Identify the blood parasite species.
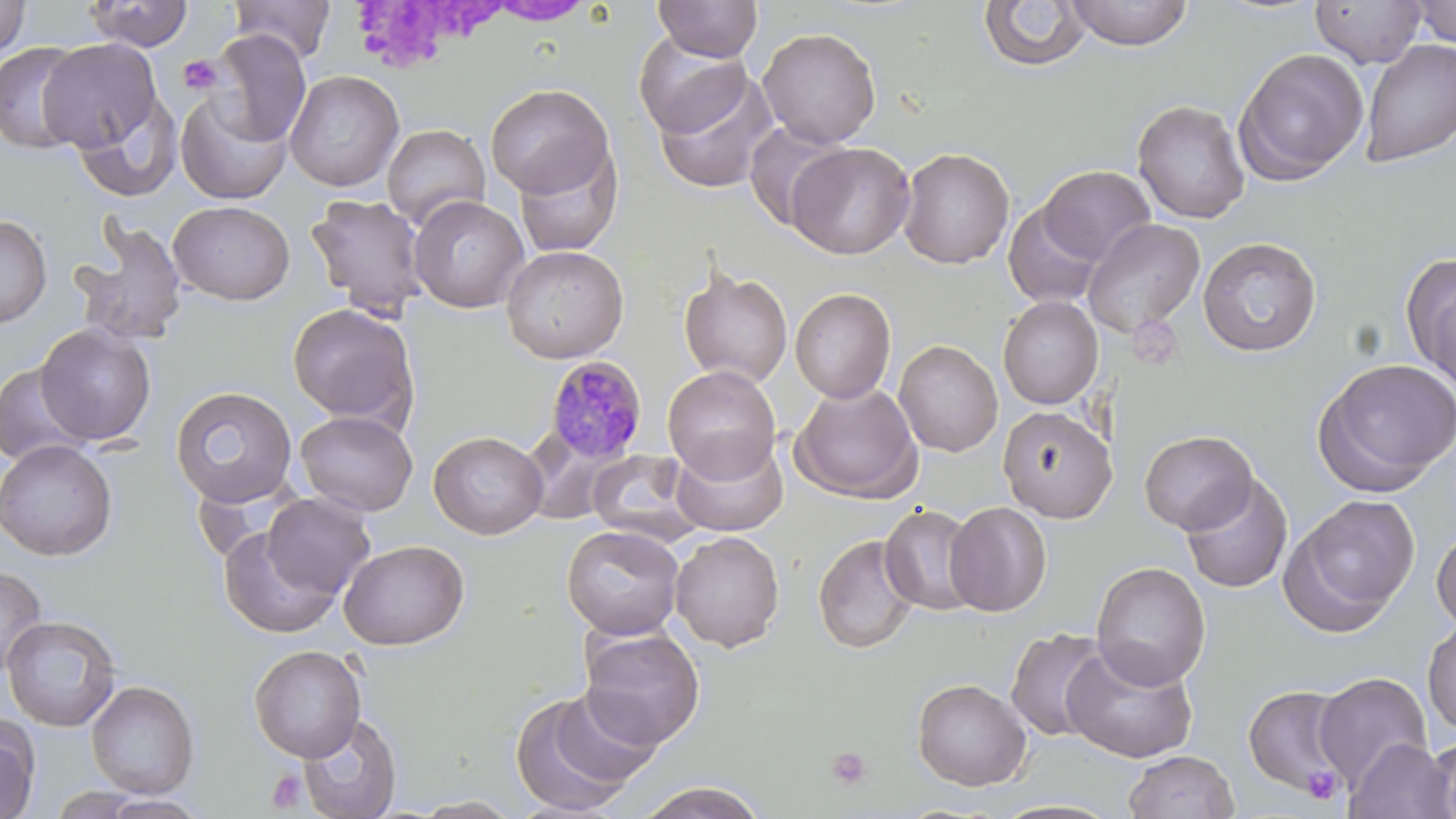
Plasmodium malariae.

platelet_locations: 'approximate bounding boxes as named x1/y1/x2/y2 corners in pixels: (x1=178, y1=54, x2=224, y2=96), (x1=826, y1=747, x2=872, y2=790), (x1=1301, y1=766, x2=1343, y2=804), (x1=267, y1=768, x2=308, y2=811)'
stain: May-Grünwald-Giemsa
modality: light microscopy
image_size: 1456×819 pixels
preparation: thin blood film
magnification: 1000x
uninfected_red_blood_cell_locations: 'approximate bounding boxes as named x1/y1/x2/y2 corners in pixels: (x1=1, y1=0, x2=33, y2=60), (x1=229, y1=0, x2=336, y2=63), (x1=653, y1=0, x2=763, y2=62), (x1=1065, y1=0, x2=1194, y2=50), (x1=1310, y1=0, x2=1427, y2=69), (x1=82, y1=1, x2=194, y2=52), (x1=484, y1=1, x2=596, y2=25), (x1=978, y1=1, x2=1093, y2=72), (x1=1408, y1=1, x2=1456, y2=49), (x1=757, y1=26, x2=881, y2=148), (x1=209, y1=29, x2=312, y2=147), (x1=633, y1=33, x2=752, y2=137), (x1=37, y1=38, x2=163, y2=155), (x1=1360, y1=39, x2=1456, y2=168), (x1=0, y1=41, x2=90, y2=155), (x1=1234, y1=47, x2=1369, y2=185), (x1=652, y1=67, x2=779, y2=195), (x1=284, y1=69, x2=404, y2=192), (x1=484, y1=83, x2=615, y2=198), (x1=175, y1=89, x2=293, y2=204), (x1=71, y1=90, x2=181, y2=203), (x1=1132, y1=99, x2=1250, y2=224), (x1=743, y1=121, x2=852, y2=234), (x1=382, y1=124, x2=491, y2=230), (x1=786, y1=142, x2=915, y2=260), (x1=512, y1=143, x2=624, y2=257), (x1=898, y1=147, x2=1015, y2=268), (x1=1037, y1=165, x2=1155, y2=266), (x1=305, y1=193, x2=430, y2=319), (x1=409, y1=195, x2=528, y2=313), (x1=168, y1=200, x2=295, y2=305), (x1=1003, y1=202, x2=1104, y2=310), (x1=0, y1=213, x2=52, y2=328), (x1=1083, y1=218, x2=1205, y2=337), (x1=70, y1=221, x2=188, y2=348), (x1=1198, y1=236, x2=1321, y2=356), (x1=501, y1=245, x2=628, y2=363), (x1=1400, y1=253, x2=1456, y2=390), (x1=678, y1=265, x2=793, y2=388), (x1=790, y1=287, x2=896, y2=403), (x1=998, y1=296, x2=1103, y2=409), (x1=288, y1=303, x2=419, y2=427), (x1=35, y1=323, x2=156, y2=446), (x1=894, y1=339, x2=1003, y2=457), (x1=1313, y1=358, x2=1456, y2=495), (x1=0, y1=363, x2=95, y2=467), (x1=662, y1=365, x2=781, y2=482), (x1=790, y1=382, x2=922, y2=503), (x1=170, y1=386, x2=297, y2=507), (x1=998, y1=405, x2=1116, y2=523), (x1=295, y1=410, x2=417, y2=516), (x1=1139, y1=429, x2=1257, y2=534), (x1=428, y1=430, x2=548, y2=539), (x1=671, y1=435, x2=788, y2=537), (x1=0, y1=440, x2=118, y2=561), (x1=586, y1=449, x2=701, y2=546), (x1=1179, y1=473, x2=1293, y2=593), (x1=261, y1=492, x2=377, y2=600), (x1=1286, y1=494, x2=1419, y2=630), (x1=944, y1=501, x2=1052, y2=617), (x1=879, y1=505, x2=982, y2=616), (x1=218, y1=524, x2=343, y2=639), (x1=561, y1=525, x2=685, y2=640), (x1=1432, y1=526, x2=1456, y2=634), (x1=670, y1=531, x2=785, y2=651), (x1=813, y1=534, x2=921, y2=655), (x1=338, y1=539, x2=469, y2=650), (x1=1091, y1=562, x2=1211, y2=690), (x1=0, y1=564, x2=48, y2=677), (x1=2, y1=615, x2=121, y2=732), (x1=1422, y1=619, x2=1456, y2=737), (x1=577, y1=625, x2=705, y2=749), (x1=1005, y1=628, x2=1113, y2=742), (x1=1062, y1=643, x2=1196, y2=762), (x1=248, y1=644, x2=367, y2=762), (x1=1313, y1=672, x2=1432, y2=790), (x1=911, y1=678, x2=1032, y2=791), (x1=86, y1=679, x2=200, y2=798), (x1=1242, y1=684, x2=1352, y2=795), (x1=508, y1=686, x2=656, y2=815), (x1=297, y1=712, x2=401, y2=819), (x1=0, y1=716, x2=39, y2=819), (x1=1422, y1=735, x2=1456, y2=819), (x1=1344, y1=737, x2=1454, y2=819), (x1=1123, y1=750, x2=1239, y2=819), (x1=632, y1=781, x2=772, y2=818), (x1=410, y1=796, x2=522, y2=817)'
field_of_view: one of a larger specimen
plasmodium_malariae_infected_red_blood_cell_locations: 'approximate bounding boxes as named x1/y1/x2/y2 corners in pixels: (x1=544, y1=355, x2=648, y2=462)'